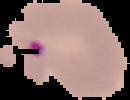

Summary:
  - Image size: 130×100 pixels
  - Image type: cell region segmented out of the field of view; surrounding area masked to black
  - Malaria status: parasitized
  - Preparation: thin blood smear